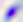

magnification: 400x
identification: Toxoplasma gondii
modality: photomicrograph